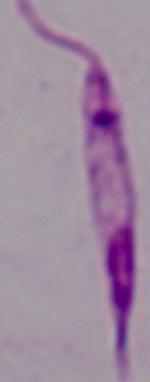
{
  "identification": "Leishmania",
  "magnification": "1000x",
  "modality": "micrograph"
}